Assess this cell for malaria.
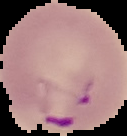
Parasitized.

From a thin blood film. Image is 127×136 pixels. Cell region segmented out of the field of view; the surrounding area is masked to black.